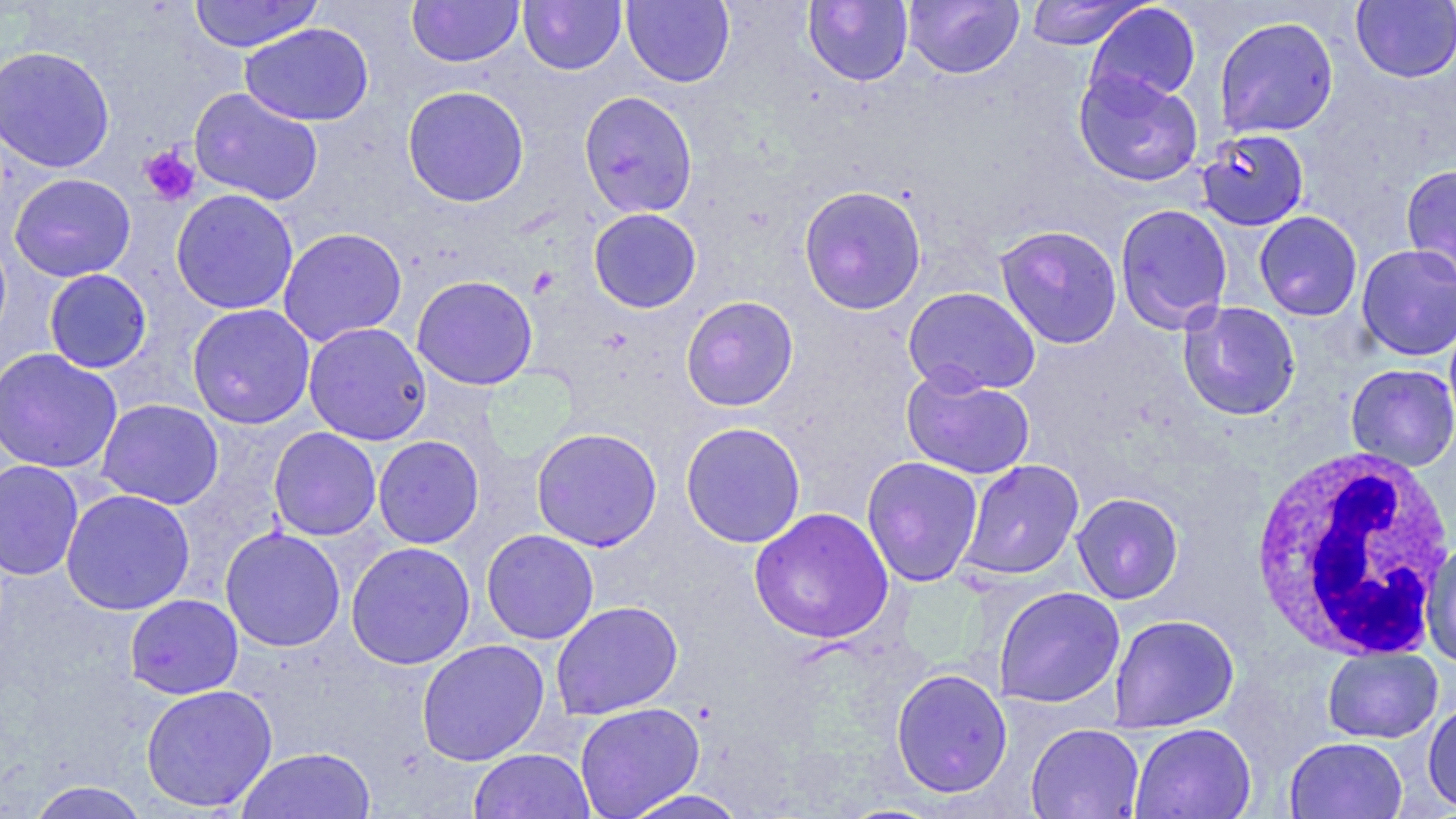

slide-level diagnosis = Plasmodium falciparum
field of view = single
preparation = thin blood film
white blood cell locations = approximate bounding boxes as named x1/y1/x2/y2 corners in pixels: (x1=1249, y1=446, x2=1455, y2=662)
image size = 1456×819 pixels
magnification = 1000x
stain = May-Grünwald-Giemsa
platelet locations = approximate bounding boxes as named x1/y1/x2/y2 corners in pixels: (x1=139, y1=145, x2=201, y2=206)
modality = optical microscopy
uninfected red blood cell locations = approximate bounding boxes as named x1/y1/x2/y2 corners in pixels: (x1=190, y1=0, x2=323, y2=52), (x1=407, y1=0, x2=524, y2=68), (x1=518, y1=0, x2=626, y2=75), (x1=621, y1=0, x2=735, y2=87), (x1=803, y1=0, x2=914, y2=86), (x1=903, y1=0, x2=1024, y2=79), (x1=1024, y1=0, x2=1150, y2=50), (x1=1351, y1=1, x2=1456, y2=84), (x1=1085, y1=2, x2=1202, y2=106), (x1=1214, y1=15, x2=1339, y2=139), (x1=240, y1=23, x2=374, y2=126), (x1=0, y1=45, x2=116, y2=173), (x1=1073, y1=69, x2=1204, y2=187), (x1=402, y1=85, x2=530, y2=207), (x1=189, y1=87, x2=323, y2=206), (x1=578, y1=90, x2=698, y2=218), (x1=1196, y1=129, x2=1310, y2=231), (x1=1400, y1=163, x2=1456, y2=284), (x1=8, y1=173, x2=136, y2=282), (x1=798, y1=184, x2=927, y2=315), (x1=171, y1=188, x2=299, y2=315), (x1=1114, y1=203, x2=1233, y2=333), (x1=588, y1=208, x2=702, y2=313), (x1=1253, y1=211, x2=1363, y2=321), (x1=995, y1=224, x2=1123, y2=349), (x1=277, y1=227, x2=408, y2=346), (x1=1356, y1=244, x2=1456, y2=360), (x1=43, y1=269, x2=153, y2=374), (x1=411, y1=274, x2=538, y2=390), (x1=903, y1=286, x2=1041, y2=396), (x1=681, y1=296, x2=799, y2=411), (x1=1177, y1=301, x2=1301, y2=420), (x1=186, y1=303, x2=316, y2=429), (x1=303, y1=322, x2=432, y2=446), (x1=0, y1=348, x2=123, y2=474), (x1=1345, y1=363, x2=1456, y2=471), (x1=900, y1=367, x2=1035, y2=480), (x1=96, y1=398, x2=224, y2=509), (x1=679, y1=421, x2=806, y2=548), (x1=268, y1=427, x2=382, y2=541), (x1=531, y1=427, x2=662, y2=551), (x1=372, y1=435, x2=485, y2=548), (x1=861, y1=456, x2=983, y2=587), (x1=0, y1=459, x2=84, y2=581), (x1=958, y1=459, x2=1084, y2=581), (x1=60, y1=489, x2=195, y2=615), (x1=1071, y1=492, x2=1184, y2=604), (x1=748, y1=506, x2=894, y2=645), (x1=220, y1=526, x2=346, y2=652), (x1=482, y1=529, x2=599, y2=644), (x1=1421, y1=540, x2=1456, y2=669), (x1=345, y1=541, x2=476, y2=669), (x1=992, y1=586, x2=1125, y2=709), (x1=124, y1=594, x2=244, y2=700), (x1=550, y1=600, x2=683, y2=720), (x1=1108, y1=614, x2=1239, y2=733), (x1=416, y1=638, x2=549, y2=766), (x1=1322, y1=647, x2=1443, y2=744), (x1=890, y1=667, x2=1013, y2=798), (x1=140, y1=683, x2=278, y2=812), (x1=1422, y1=698, x2=1456, y2=815), (x1=574, y1=702, x2=705, y2=819), (x1=1129, y1=722, x2=1256, y2=819), (x1=1025, y1=724, x2=1144, y2=819), (x1=1284, y1=736, x2=1408, y2=818), (x1=237, y1=747, x2=376, y2=819), (x1=469, y1=748, x2=595, y2=819), (x1=26, y1=781, x2=151, y2=819), (x1=618, y1=789, x2=752, y2=819)